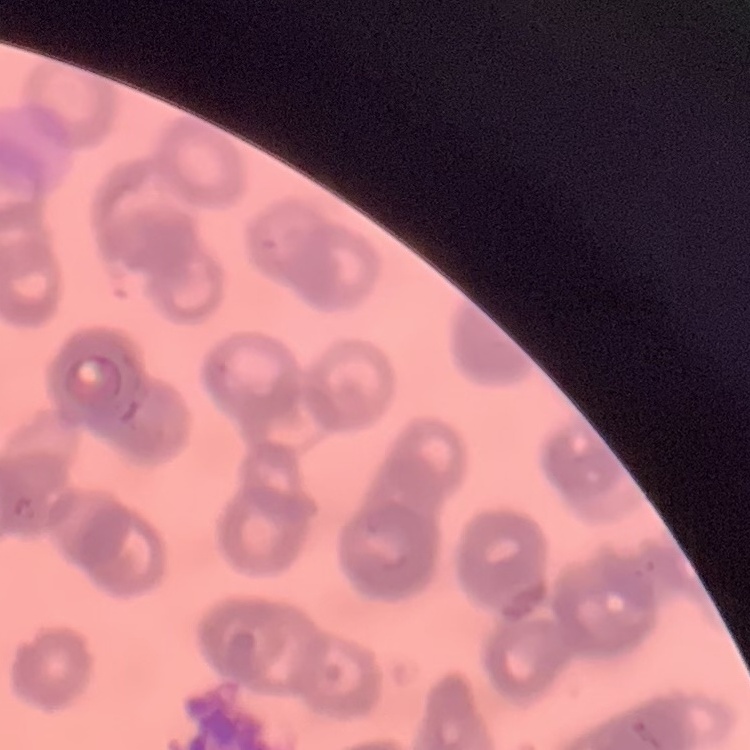

erythrocyte morphology = rouleaux formation
image type = one tile cut from a larger photomicrograph
stain = Field's or Giemsa
preparation = thin peripheral smear